Assess the morphology of the red blood cells.
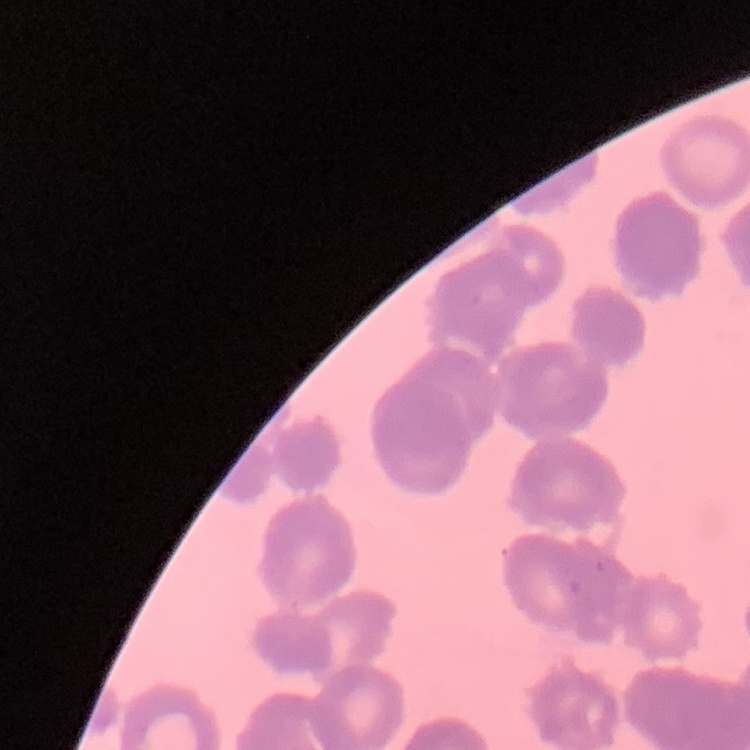
Rouleaux formation.

Stained with either Field's or Giemsa. Thin peripheral smear. One tile cut from a larger photomicrograph.